Describe the morphology of the red blood cells.
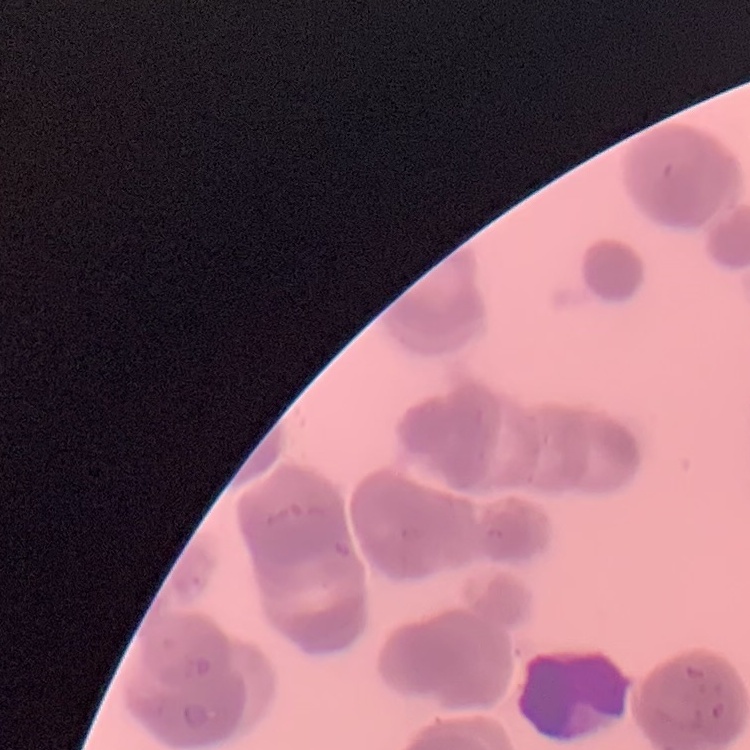
Rouleaux formation.

Field's or Giemsa stain. One tile cut from a larger photomicrograph. Thin blood smear.